Report the malaria status of this cell.
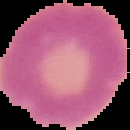

Uninfected.

The area outside the segmented cell region is set to black. From a thin blood film. Image is 130×130 pixels.